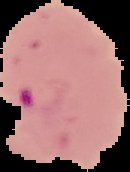

{
  "preparation": "thin blood film",
  "image_size": "130×172 pixels",
  "image_type": "segmented cell region with the area outside set to black",
  "malaria_status": "parasitized"
}